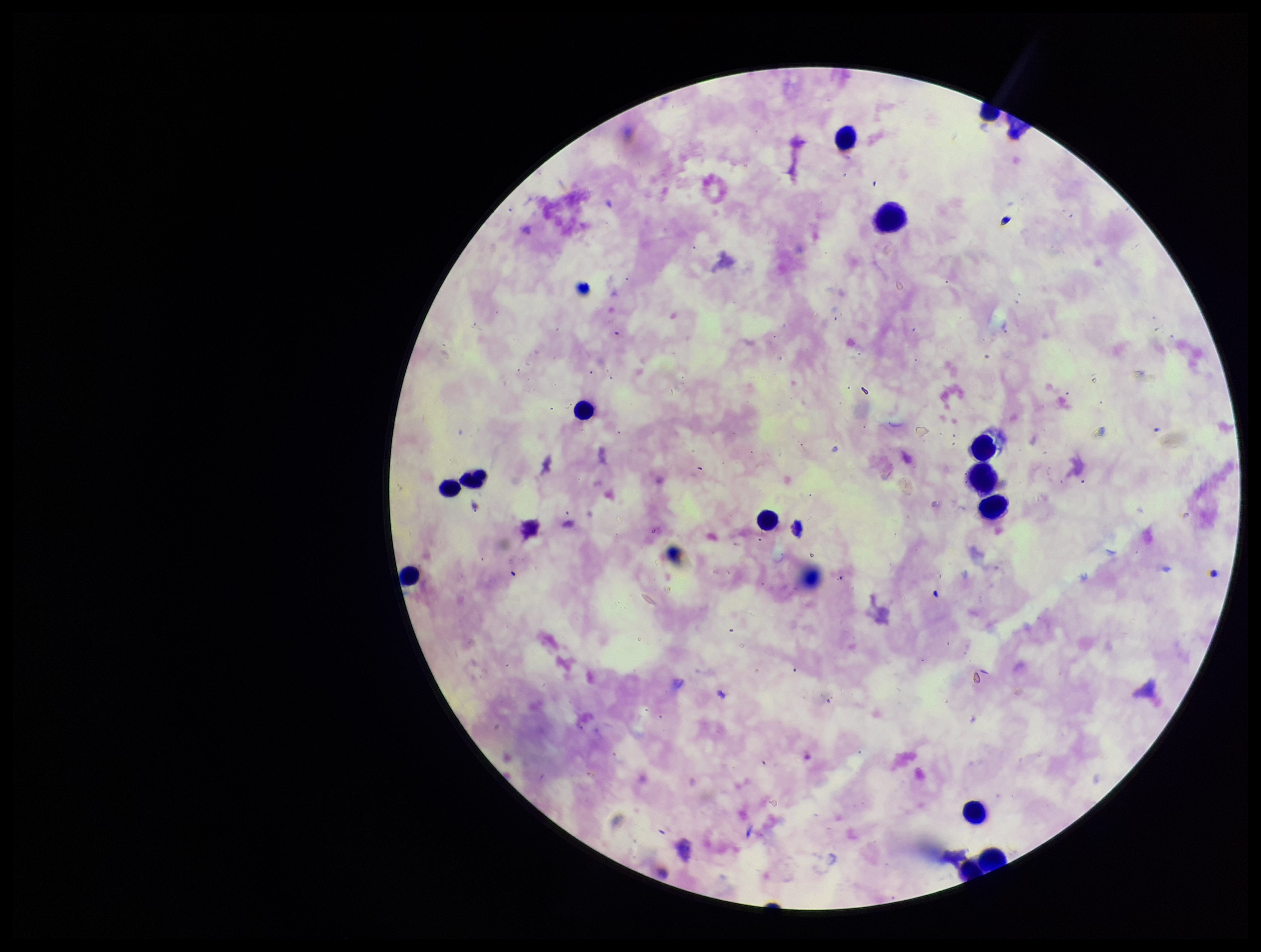

Summary:
  - Preparation: thick
  - Capture: smartphone photograph through the microscope eyepiece
  - Leukocyte count: 12
  - Species reported for this patient: Plasmodium falciparum
  - Patient malaria status: positive
  - Plasmodium parasites: none detected
  - Parasite count: 0
  - Field of view: one from this slide
  - Stain: Giemsa
  - Image size: 1261×952 pixels